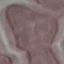
malaria status = uninfected
image type = automatically extracted cell patch, resized to 64 × 64 pixels
stain = Giemsa
capture = smartphone through the microscope eyepiece
preparation = thin blood smear